State which parasite is depicted.
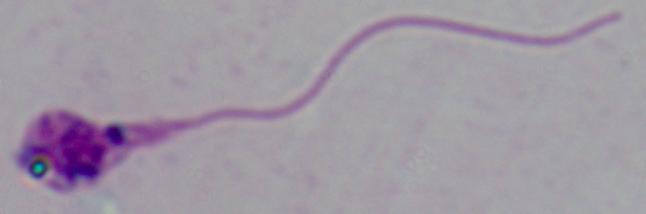
This is Leishmania.

Captured at 1000x magnification. Photomicrograph.